Identify the parasite.
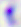
Toxoplasma gondii.

Summary:
  - Modality: photomicrograph
  - Magnification: 400x